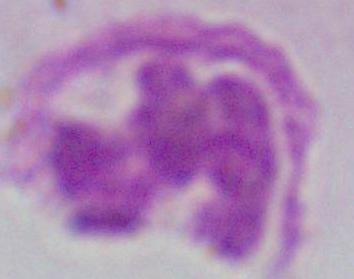
A white blood cell is shown. Captured at 1000x magnification. Micrograph.